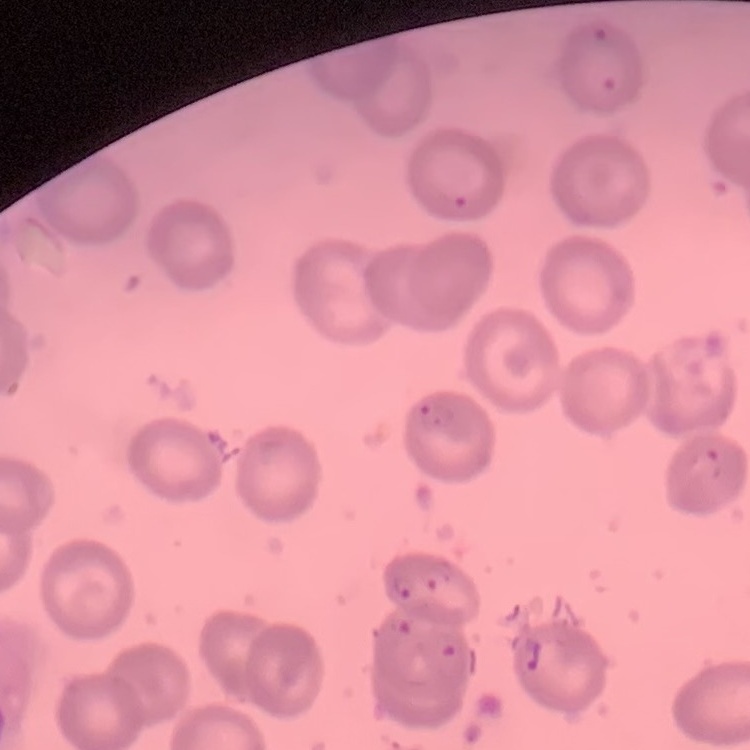 The erythrocytes show no rouleaux formation. Thin blood smear. Stained with either Field's or Giemsa. Square crop of a larger photomicrograph.